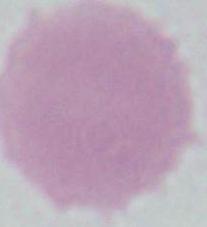
An erythrocyte is seen. 1000x magnification. Micrograph.